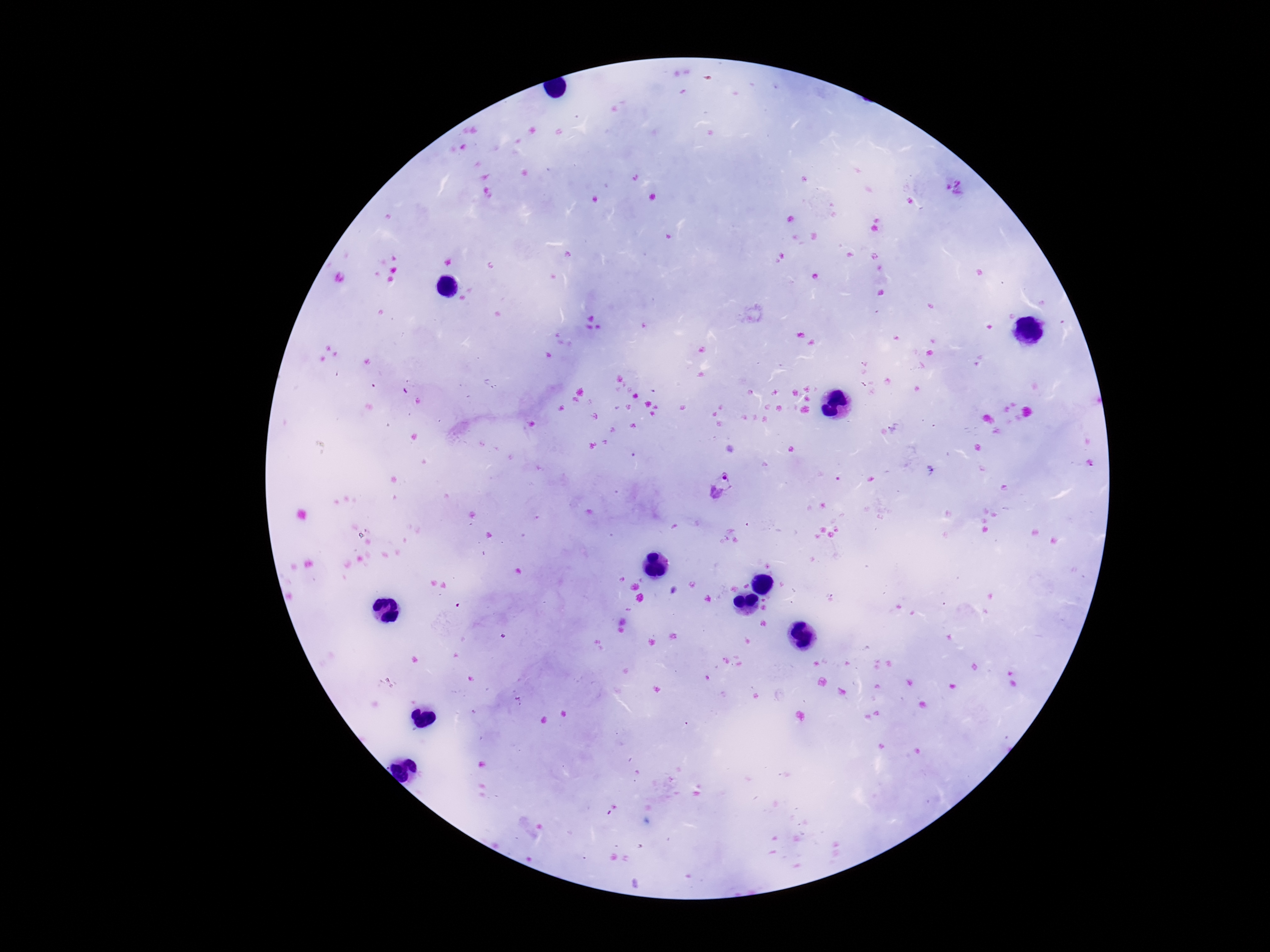
field of view = one from this slide
magnification = 100x
preparation = thick blood smear
stain = Giemsa
patient malaria status = positive
Plasmodium parasite locations = approximate centers as [x, y] in pixels: [722, 486]
image size = 1270×952 pixels
capture = smartphone camera through the microscope eyepiece